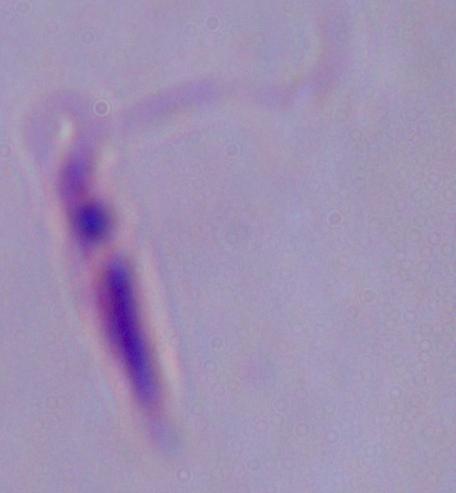
Summary:
  - Magnification: 1000x
  - Identification: Leishmania
  - Modality: micrograph